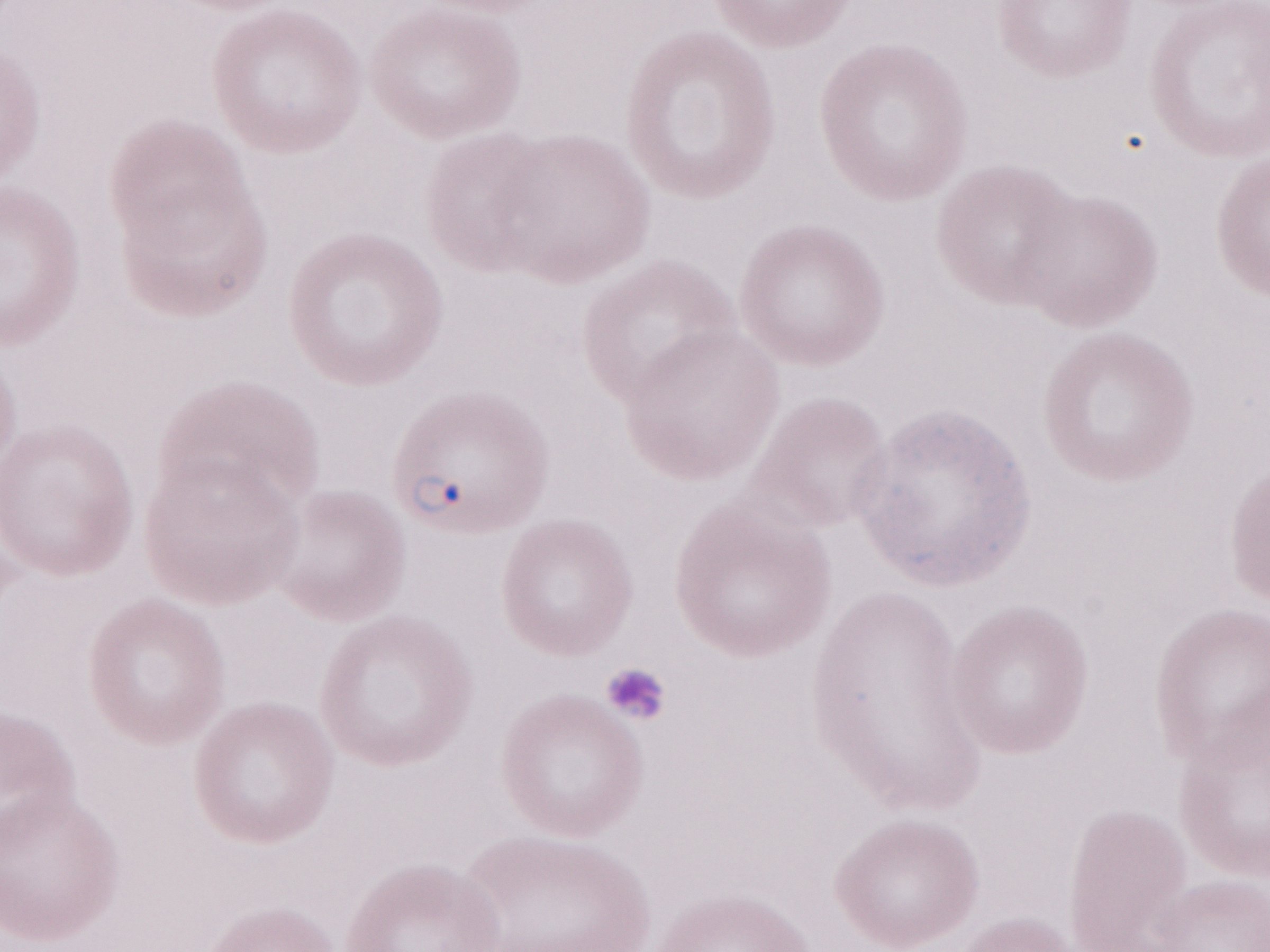
Thin peripheral-blood smear. Image is 1270×952 pixels. May-Grünwald-Giemsa-stained preparation. Olympus BX43 microscope, Olympus DP73 camera. Single field of view. 1,000x magnification. Patient-level malaria diagnosis: positive.